Name the parasite shown.
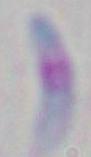
This is Toxoplasma gondii.

modality = photomicrograph
magnification = 1000x